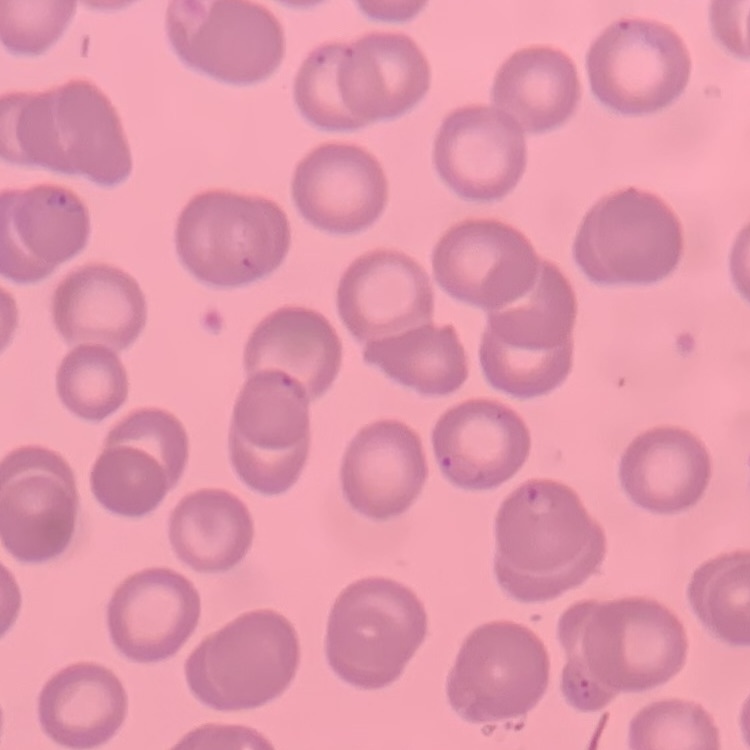
The red blood cells show no rouleaux formation. Thin blood smear. One tile cut from a larger photomicrograph. Stained with either Field's or Giemsa.